Assess this cell for malaria.
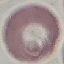

Uninfected.

Thin blood film. Giemsa-stained preparation. Photographed with a smartphone camera at the microscope eyepiece. Cell patch, automatically extracted from a larger field of view and resized to 64 × 64 pixels.